Point out each malaria parasite.
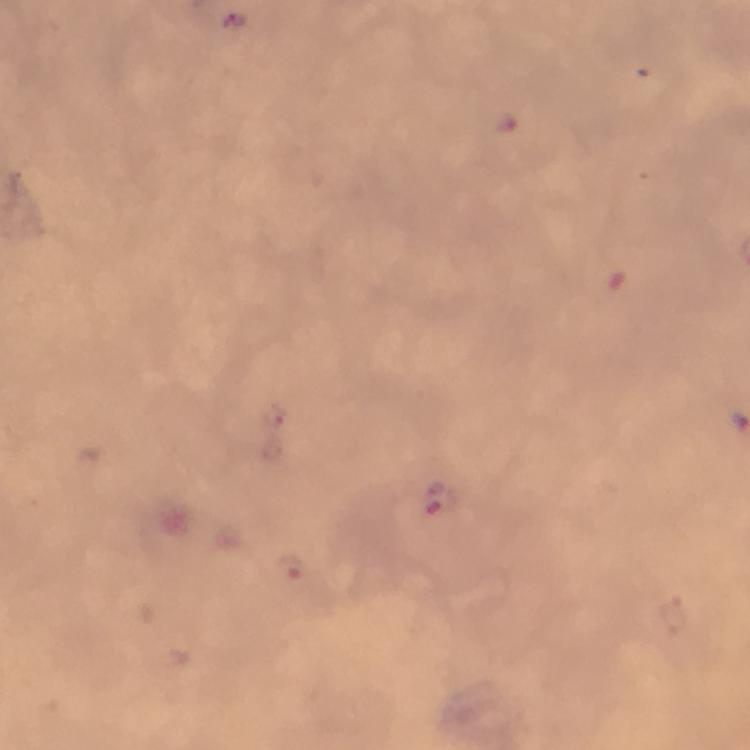
Approximate centers as (x, y) in pixels.
Malaria parasites: (235, 20), (504, 125), (437, 500).

Summary:
  - Stain: Giemsa
  - Image size: 750×750 pixels
  - Capture: smartphone camera through the microscope
  - Magnification: 100x
  - Preparation: thick blood smear
  - Cropped from: one field of view
  - Context: from a diagnostic examination for malaria
  - Immersion oil: applied